Point out each Plasmodium parasite.
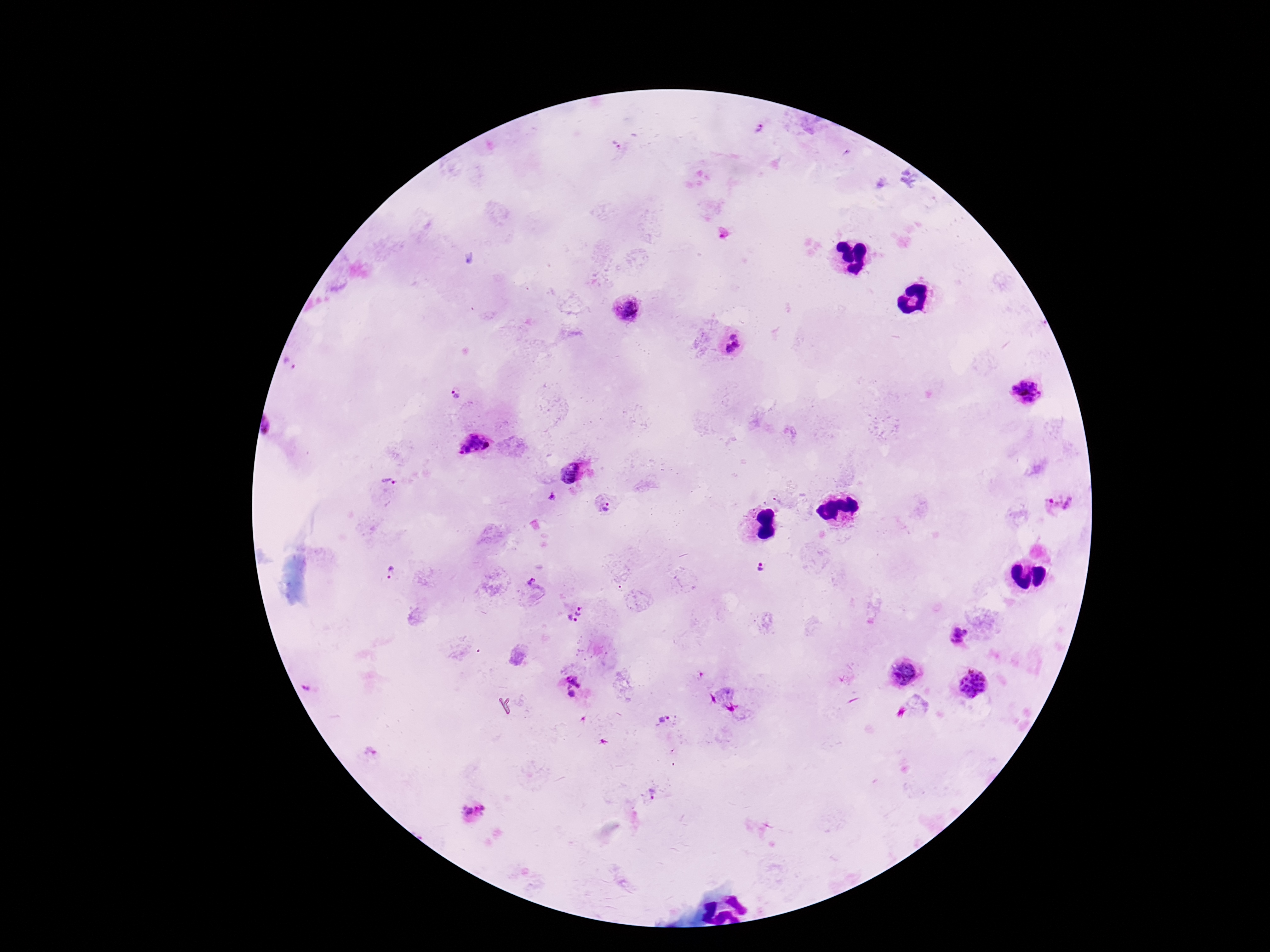

Approximate centers as [x, y] in pixels.
Plasmodium parasites: [759, 129], [616, 144], [470, 259], [627, 309], [732, 335], [736, 344], [729, 349], [289, 364], [1026, 392], [454, 393], [472, 444], [569, 472], [389, 481], [552, 496], [1060, 504], [606, 509], [762, 568], [392, 571], [531, 581], [579, 608], [578, 614], [570, 617], [575, 620], [959, 636], [904, 673], [574, 680], [973, 683], [305, 689], [572, 693], [665, 720], [370, 753], [652, 794], [475, 811].

magnification = 100x
capture = smartphone camera through the microscope eyepiece
preparation = thick blood smear
image size = 1270×952 pixels
field of view = one from this slide
stain = Giemsa
patient malaria status = infected